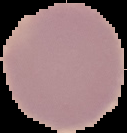
image_size: 127×133 pixels
preparation: thin blood smear
result: no Plasmodium parasites detected
image_type: segmented cell region with the area outside set to black